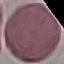
result = no malaria parasites detected
image type = cell patch, automatically extracted from a larger field of view and resized to 64 × 64 pixels
stain = Giemsa
capture = smartphone camera at the microscope eyepiece
preparation = thin blood film